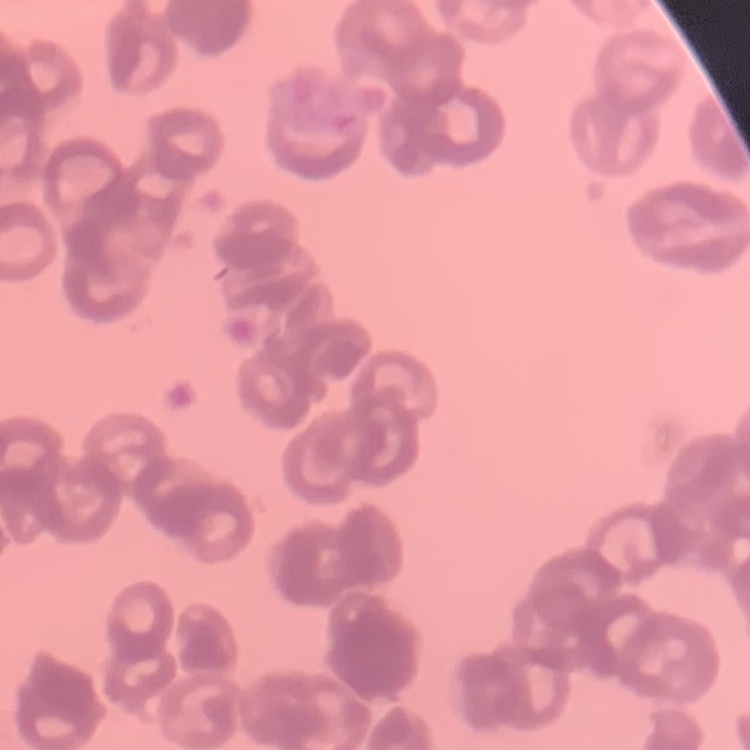 The red blood cells show rouleaux formation. Thin blood smear. Stained with either Field's or Giemsa. Square crop of a larger photomicrograph.